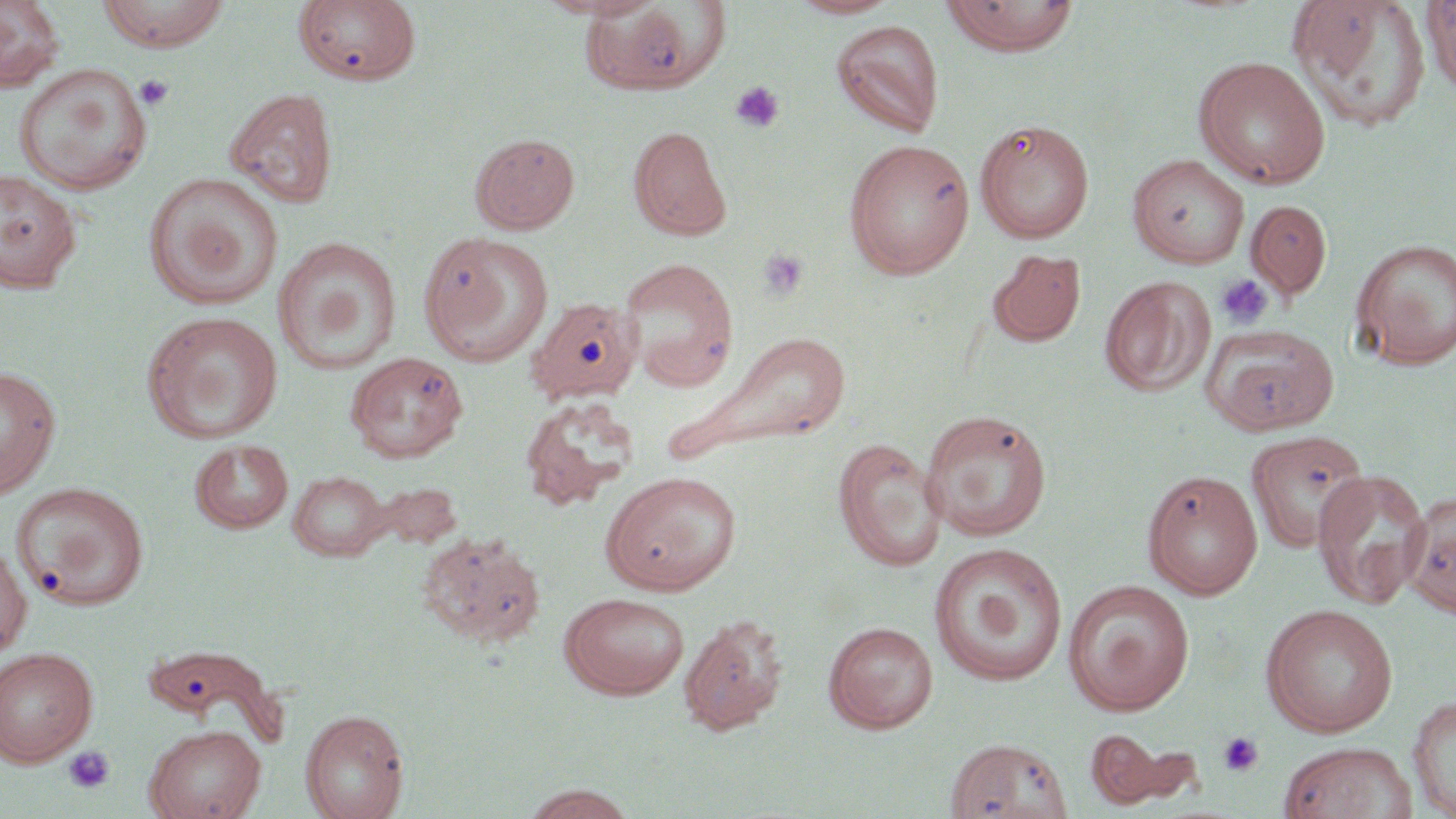 Approximate bounding boxes as named x1/y1/x2/y2 corners in pixels. Platelet locations: (x1=134, y1=74, x2=174, y2=111), (x1=730, y1=81, x2=785, y2=133), (x1=756, y1=248, x2=810, y2=301), (x1=1215, y1=274, x2=1273, y2=330), (x1=1218, y1=731, x2=1264, y2=777), (x1=63, y1=746, x2=116, y2=794). Uninfected red blood cell locations: (x1=0, y1=0, x2=66, y2=92), (x1=95, y1=0, x2=231, y2=52), (x1=534, y1=0, x2=657, y2=19), (x1=787, y1=0, x2=900, y2=19), (x1=941, y1=0, x2=1080, y2=55), (x1=1286, y1=0, x2=1431, y2=133), (x1=1421, y1=0, x2=1455, y2=96), (x1=294, y1=1, x2=421, y2=86), (x1=581, y1=1, x2=718, y2=95), (x1=830, y1=20, x2=945, y2=138), (x1=1193, y1=55, x2=1331, y2=189), (x1=13, y1=63, x2=153, y2=196), (x1=225, y1=87, x2=339, y2=209), (x1=974, y1=118, x2=1095, y2=244), (x1=628, y1=125, x2=732, y2=241), (x1=469, y1=132, x2=581, y2=234), (x1=843, y1=139, x2=975, y2=279), (x1=1127, y1=154, x2=1250, y2=269), (x1=0, y1=169, x2=82, y2=295), (x1=143, y1=172, x2=284, y2=310), (x1=1246, y1=199, x2=1333, y2=299), (x1=419, y1=231, x2=553, y2=363), (x1=272, y1=237, x2=402, y2=376), (x1=1350, y1=237, x2=1456, y2=369), (x1=986, y1=248, x2=1087, y2=348), (x1=617, y1=257, x2=740, y2=390), (x1=1100, y1=276, x2=1215, y2=397), (x1=530, y1=301, x2=649, y2=408), (x1=142, y1=311, x2=284, y2=444), (x1=1202, y1=323, x2=1339, y2=435), (x1=678, y1=330, x2=853, y2=459), (x1=344, y1=351, x2=469, y2=464), (x1=0, y1=365, x2=61, y2=499), (x1=519, y1=397, x2=640, y2=510), (x1=919, y1=409, x2=1053, y2=541), (x1=1245, y1=429, x2=1370, y2=554), (x1=832, y1=438, x2=948, y2=571), (x1=190, y1=439, x2=294, y2=534), (x1=1312, y1=467, x2=1432, y2=609), (x1=288, y1=469, x2=390, y2=561), (x1=1142, y1=469, x2=1264, y2=600), (x1=600, y1=470, x2=742, y2=595), (x1=12, y1=482, x2=149, y2=610), (x1=1403, y1=489, x2=1456, y2=617), (x1=417, y1=530, x2=547, y2=649), (x1=0, y1=540, x2=32, y2=658), (x1=929, y1=542, x2=1068, y2=687), (x1=1062, y1=580, x2=1195, y2=715), (x1=558, y1=592, x2=690, y2=699), (x1=1260, y1=603, x2=1399, y2=737), (x1=679, y1=613, x2=790, y2=735), (x1=824, y1=620, x2=938, y2=732), (x1=143, y1=642, x2=284, y2=743), (x1=0, y1=646, x2=99, y2=767), (x1=1407, y1=695, x2=1456, y2=817), (x1=300, y1=708, x2=409, y2=819), (x1=144, y1=724, x2=266, y2=819), (x1=1086, y1=729, x2=1173, y2=808), (x1=944, y1=736, x2=1073, y2=819), (x1=1277, y1=741, x2=1417, y2=819), (x1=520, y1=783, x2=639, y2=819). Slide-level diagnosis: negative for blood parasites. May-Grünwald-Giemsa stain. 1000x magnification. Image is 1456×819 pixels. Light microscopy. One field of a larger specimen. Thin blood film.